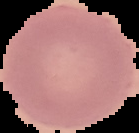
Summary:
  - Preparation: thin blood film
  - Malaria status: uninfected
  - Image size: 139×133 pixels
  - Image type: cell region segmented out of the field of view; surrounding area masked to black